Point out each Plasmodium parasite.
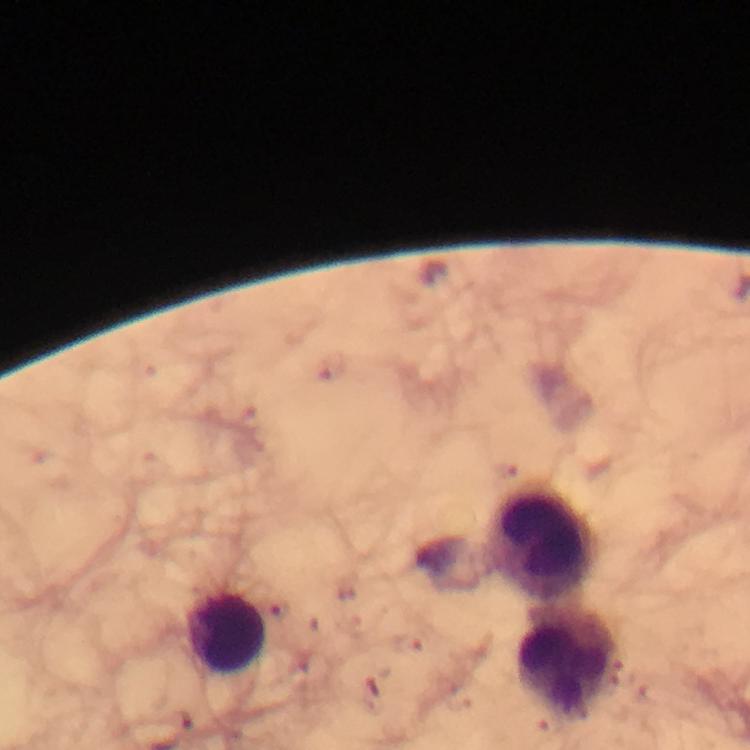

No Plasmodium parasites detected.

Approximate centers as [x, y] in pixels. Leukocyte locations: [545, 541], [227, 634], [570, 665]. Photographed with a smartphone mounted on the microscope. Image is 750×750 pixels. Immersion oil was used. Thick blood film. Cropped region of a single field of view. From a malaria diagnostic workup. At 100x magnification. Giemsa-stained preparation.